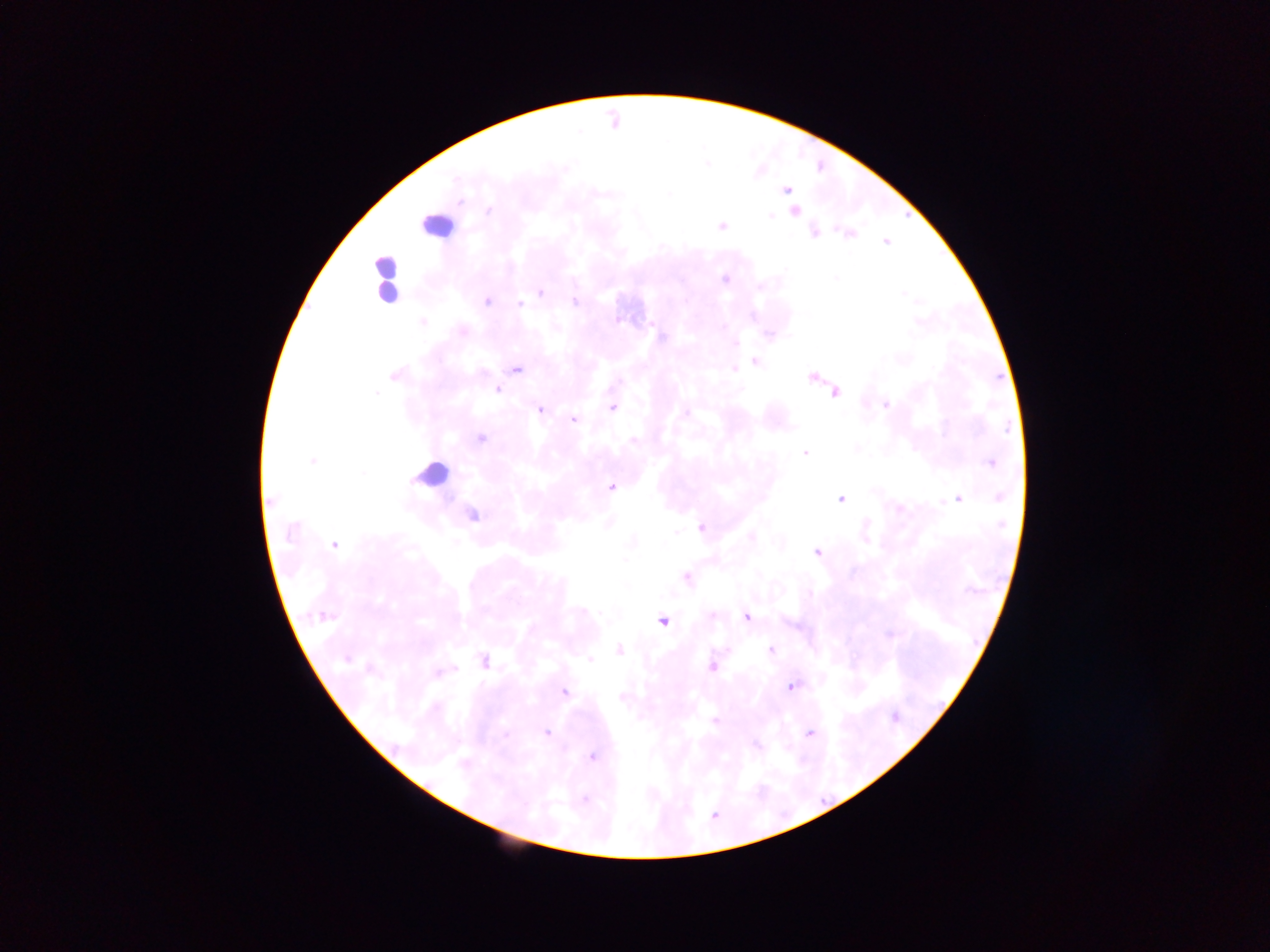 Approximate centers as {x, y} in pixels. Plasmodium parasite locations: {785, 190}, {486, 300}, {519, 305}, {516, 371}, {497, 390}, {885, 405}, {612, 408}, {541, 409}, {574, 419}, {633, 442}, {803, 453}, {990, 463}, {611, 486}, {998, 497}, {957, 498}, {839, 499}, {273, 502}, {701, 527}, {337, 545}, {816, 550}, {686, 578}, {747, 617}, {661, 622}, {770, 649}, {620, 650}, {712, 668}, {790, 687}, {564, 692}, {547, 733}, {504, 734}, {811, 735}, {592, 756}, {583, 798}. Leukocyte locations: {434, 217}, {384, 286}, {428, 473}. One field of view. Image is 1270×952 pixels. Thick blood film. Collected in Ghana. Photographed through a microscope with a mobile-phone camera.